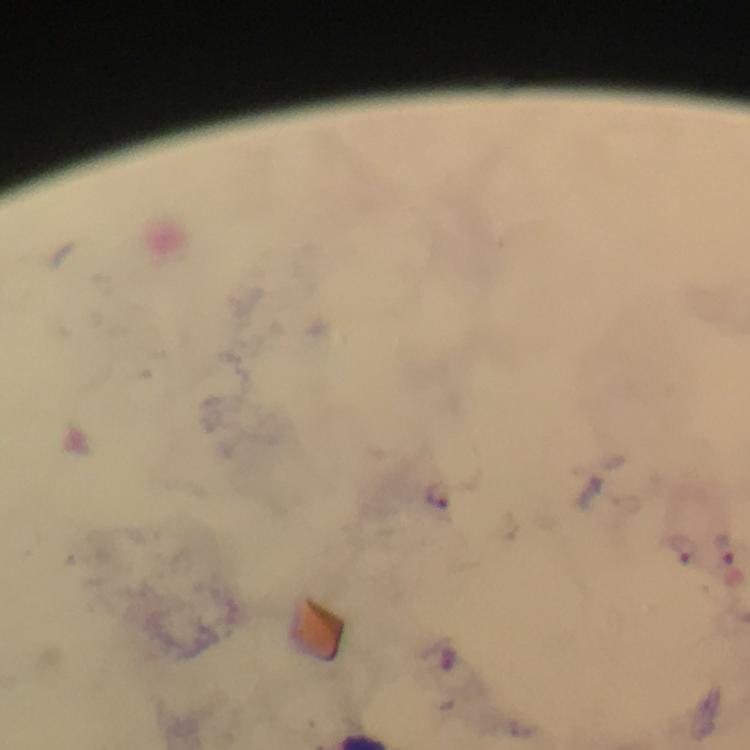

Approximate centers as [x, y] in pixels.
Summary:
  - Plasmodium parasite locations: [438, 494], [728, 548], [684, 549]
  - Magnification: 100x
  - Cropped from: a single field of view
  - Immersion oil: used
  - Capture: smartphone photograph through a microscope
  - Context: from a diagnostic examination for malaria
  - Preparation: thick blood smear
  - Image size: 750×750 pixels
  - Stain: Giemsa